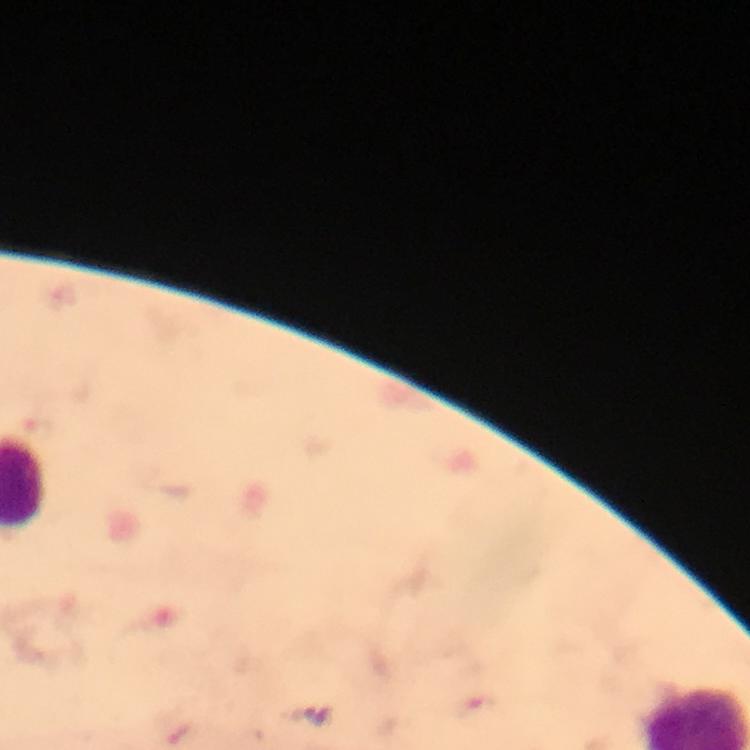
{
  "capture": "smartphone mounted on the microscope",
  "context": "from a malaria diagnostic workup",
  "plasmodium_parasite_locations": "approximate centers as {x, y} in pixels: {479, 704}",
  "immersion_oil": "applied",
  "preparation": "thick smear",
  "magnification": "100x",
  "image_size": "750×750 pixels",
  "cropped_from": "a single field of view",
  "stain": "Giemsa"
}